Describe the morphology of the erythrocytes.
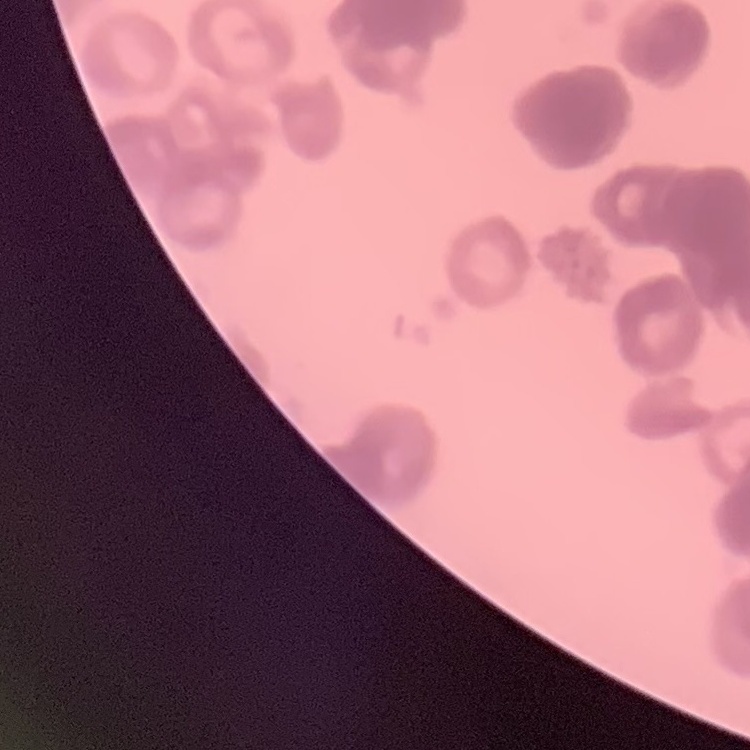
Rouleaux formation.

Square crop of a larger photomicrograph. Thin peripheral smear. Field's or Giemsa stain.